Outline each blood parasite and name the species.
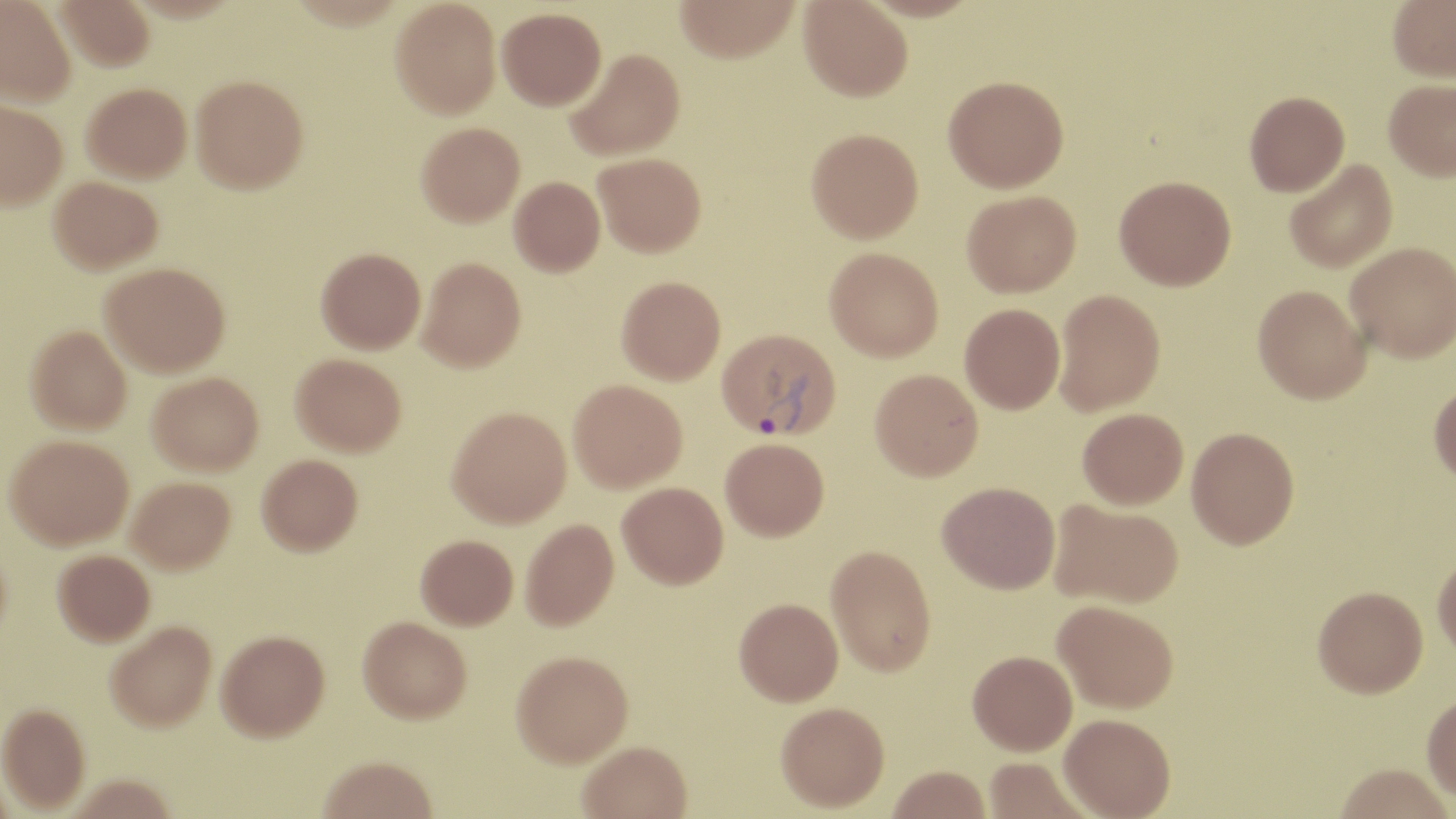

Approximate bounding boxes as named x1/y1/x2/y2 corners in pixels.
Plasmodium vivax-infected red blood cells: (x1=717, y1=328, x2=841, y2=441).
No Plasmodium falciparum, Plasmodium ovale, Plasmodium malariae, Babesia divergens, or Trypanosoma brucei observed.

{
  "slide_level_diagnosis": "Plasmodium vivax",
  "image_size": "1456×819 pixels",
  "uninfected_red_blood_cell_locations": "approximate bounding boxes as named x1/y1/x2/y2 corners in pixels: (x1=0, y1=0, x2=75, y2=106), (x1=55, y1=0, x2=156, y2=71), (x1=390, y1=0, x2=501, y2=119), (x1=675, y1=0, x2=800, y2=62), (x1=858, y1=0, x2=983, y2=22), (x1=1387, y1=0, x2=1456, y2=81), (x1=799, y1=1, x2=912, y2=101), (x1=497, y1=7, x2=606, y2=110), (x1=566, y1=48, x2=685, y2=160), (x1=191, y1=75, x2=309, y2=194), (x1=943, y1=75, x2=1069, y2=192), (x1=1383, y1=78, x2=1456, y2=181), (x1=81, y1=83, x2=192, y2=182), (x1=1244, y1=90, x2=1349, y2=196), (x1=0, y1=99, x2=67, y2=210), (x1=416, y1=121, x2=525, y2=226), (x1=806, y1=127, x2=923, y2=243), (x1=594, y1=152, x2=706, y2=257), (x1=1284, y1=159, x2=1398, y2=273), (x1=1114, y1=175, x2=1236, y2=290), (x1=49, y1=176, x2=163, y2=274), (x1=509, y1=176, x2=605, y2=276), (x1=962, y1=190, x2=1081, y2=297), (x1=1345, y1=242, x2=1456, y2=361), (x1=316, y1=247, x2=426, y2=353), (x1=825, y1=247, x2=943, y2=361), (x1=418, y1=257, x2=526, y2=371), (x1=100, y1=262, x2=230, y2=377), (x1=617, y1=275, x2=725, y2=384), (x1=1252, y1=285, x2=1370, y2=404), (x1=1053, y1=289, x2=1166, y2=415), (x1=959, y1=303, x2=1066, y2=413), (x1=25, y1=324, x2=132, y2=434), (x1=291, y1=352, x2=406, y2=456), (x1=870, y1=368, x2=983, y2=481), (x1=148, y1=371, x2=264, y2=475), (x1=568, y1=379, x2=686, y2=492), (x1=1429, y1=381, x2=1456, y2=486), (x1=447, y1=406, x2=572, y2=527), (x1=1077, y1=408, x2=1188, y2=509), (x1=1186, y1=427, x2=1300, y2=549), (x1=5, y1=434, x2=133, y2=549), (x1=720, y1=437, x2=829, y2=541), (x1=257, y1=453, x2=362, y2=555), (x1=127, y1=477, x2=235, y2=573), (x1=937, y1=481, x2=1060, y2=593), (x1=617, y1=482, x2=728, y2=589), (x1=1049, y1=499, x2=1183, y2=609), (x1=521, y1=518, x2=619, y2=630), (x1=416, y1=534, x2=518, y2=629), (x1=0, y1=536, x2=13, y2=654), (x1=825, y1=544, x2=937, y2=676), (x1=53, y1=549, x2=155, y2=645), (x1=1432, y1=550, x2=1456, y2=660), (x1=1313, y1=585, x2=1428, y2=697), (x1=734, y1=598, x2=843, y2=705), (x1=1053, y1=600, x2=1178, y2=713), (x1=358, y1=616, x2=472, y2=723), (x1=105, y1=620, x2=216, y2=731), (x1=216, y1=629, x2=330, y2=740), (x1=511, y1=650, x2=633, y2=767), (x1=968, y1=650, x2=1077, y2=755), (x1=1421, y1=692, x2=1456, y2=804), (x1=775, y1=701, x2=890, y2=812), (x1=0, y1=703, x2=90, y2=812), (x1=1059, y1=713, x2=1176, y2=818), (x1=577, y1=741, x2=692, y2=819), (x1=983, y1=755, x2=1095, y2=818), (x1=317, y1=756, x2=438, y2=819), (x1=1333, y1=763, x2=1453, y2=819), (x1=887, y1=765, x2=991, y2=819)",
  "field_of_view": "one of a larger specimen",
  "magnification": "1000x",
  "stain": "May-Grünwald-Giemsa",
  "modality": "optical microscopy",
  "preparation": "thin blood film"
}